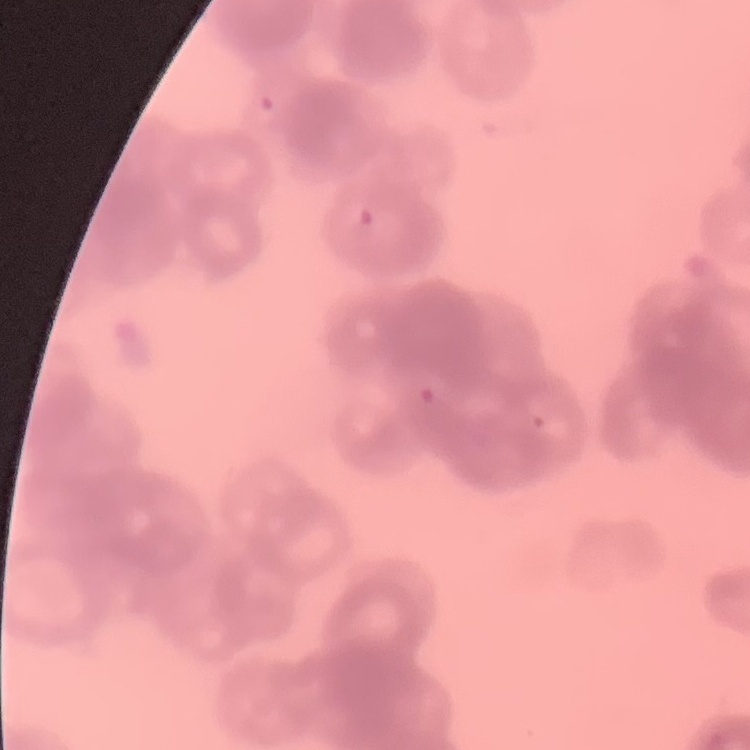
red blood cell morphology = rouleaux formation
preparation = thin blood film
image type = one tile cut from a larger photomicrograph
stain = Field's or Giemsa